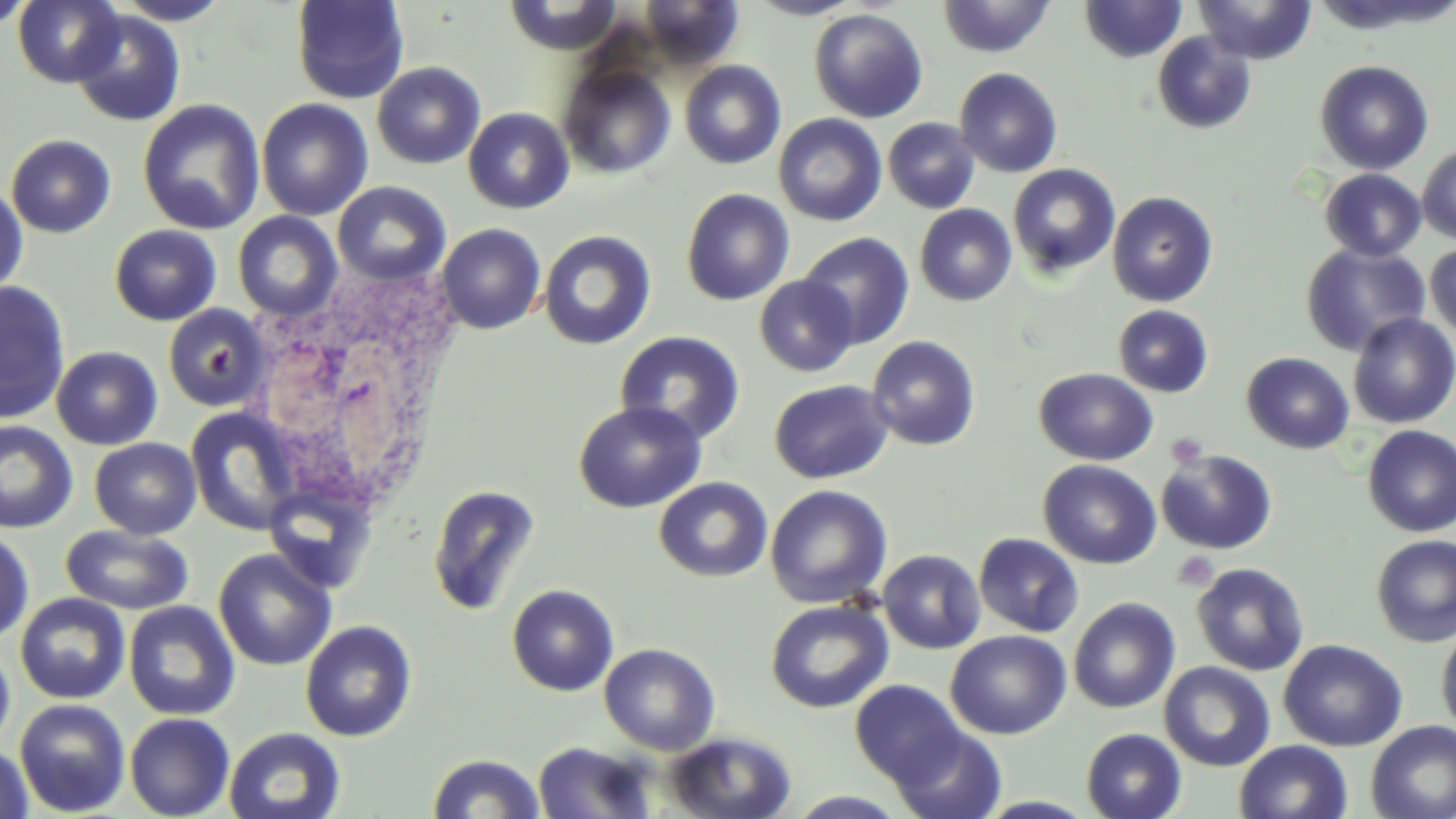
Summary:
  - Coordinate format: approximate bounding boxes as (x1, y1, x2, y2) in pixels
  - Platelet locations: (1166, 433, 1209, 468), (1172, 551, 1219, 591)
  - Uninfected red blood cell locations: (0, 0, 35, 35), (12, 0, 125, 87), (111, 0, 234, 25), (290, 0, 410, 104), (500, 0, 627, 57), (635, 0, 744, 70), (746, 0, 865, 20), (937, 0, 1057, 58), (1195, 0, 1317, 64), (1079, 1, 1188, 63), (809, 8, 928, 123), (70, 9, 186, 127), (1152, 31, 1257, 134), (679, 60, 786, 169), (1315, 60, 1434, 175), (372, 61, 486, 169), (559, 63, 676, 180), (954, 67, 1064, 178), (137, 99, 265, 235), (256, 99, 373, 221), (463, 107, 575, 214), (774, 114, 887, 226), (883, 117, 980, 213), (5, 134, 117, 238), (1417, 142, 1456, 244), (1007, 163, 1121, 279), (1320, 169, 1426, 261), (0, 181, 29, 300), (332, 181, 452, 287), (681, 188, 795, 306), (1107, 191, 1219, 307), (915, 204, 1017, 306), (232, 211, 343, 321), (436, 223, 546, 334), (109, 224, 222, 326), (538, 230, 656, 350), (798, 232, 914, 350), (1300, 242, 1430, 356), (1425, 242, 1456, 345), (755, 275, 859, 376), (0, 280, 71, 424), (163, 304, 270, 410), (1113, 304, 1213, 397), (1348, 313, 1456, 428), (614, 330, 746, 445), (867, 335, 981, 451), (51, 346, 163, 450), (1242, 352, 1355, 454), (1034, 367, 1157, 465), (769, 379, 894, 484), (573, 400, 706, 514), (185, 406, 302, 538), (0, 421, 78, 534), (1362, 425, 1456, 537), (89, 437, 201, 539), (1156, 448, 1277, 554), (1038, 459, 1161, 569), (654, 477, 773, 583), (427, 484, 541, 616), (765, 484, 892, 609), (59, 525, 193, 615), (0, 528, 35, 645), (973, 532, 1084, 637), (1372, 533, 1456, 647), (213, 549, 337, 671), (878, 549, 986, 654), (1191, 562, 1309, 676), (506, 584, 619, 696), (15, 592, 130, 704), (1068, 597, 1180, 713), (765, 599, 893, 714), (123, 600, 240, 721), (300, 620, 417, 742), (1436, 622, 1456, 739), (945, 630, 1071, 739), (1278, 639, 1408, 752), (599, 642, 720, 755), (0, 643, 15, 755), (1159, 661, 1275, 772), (850, 679, 966, 786), (14, 698, 130, 816), (125, 712, 235, 819), (1366, 720, 1456, 818), (888, 724, 1007, 819), (223, 727, 346, 819), (1081, 728, 1186, 819), (664, 730, 798, 819), (1234, 739, 1353, 819), (532, 741, 656, 819), (0, 743, 34, 819), (427, 752, 545, 819), (786, 790, 911, 818)
  - White blood cell locations: (249, 265, 462, 523)
  - Slide-level diagnosis: no evidence of blood parasites
  - Stain: May-Grünwald-Giemsa
  - Field of view: one of a larger specimen
  - Magnification: 1000x
  - Preparation: thin blood smear
  - Modality: optical microscopy
  - Image size: 1456×819 pixels